Classify this cell by malaria status.
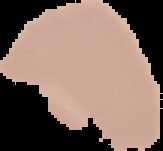
Uninfected.

Summary:
  - Image type: segmented cell region with the area outside set to black
  - Image size: 163×151 pixels
  - Preparation: thin blood smear